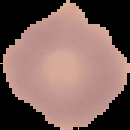

Image is 130×130 pixels. From a thin blood film. Cell region segmented out of the field of view; the surrounding area is masked to black. Result: no Plasmodium parasites seen.